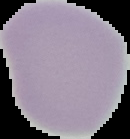
Image is 130×139 pixels. Segmented cell region on a black background. Result: no malaria parasites detected. From a thin blood smear.